Give the position of every malaria parasite.
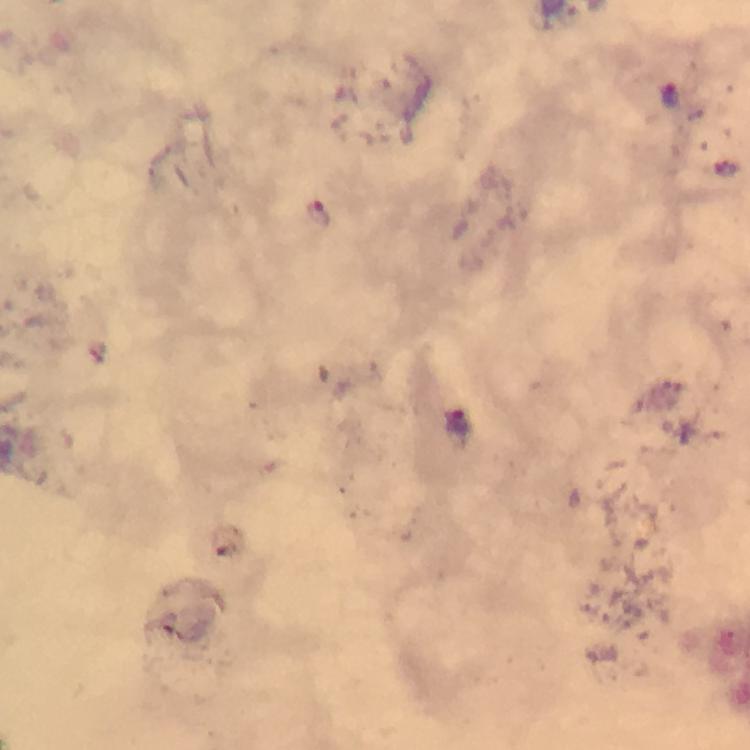

Approximate object centers, in pixels from the top-left corner.
Malaria parasites: (x=321, y=214).

Summary:
  - Image size: 750×750 pixels
  - Context: from a diagnostic examination for malaria
  - Immersion oil: used
  - Stain: Giemsa
  - Preparation: thick blood smear
  - Magnification: 100x
  - Cropped from: one field of view
  - Capture: smartphone mounted on the microscope